Assess for malaria.
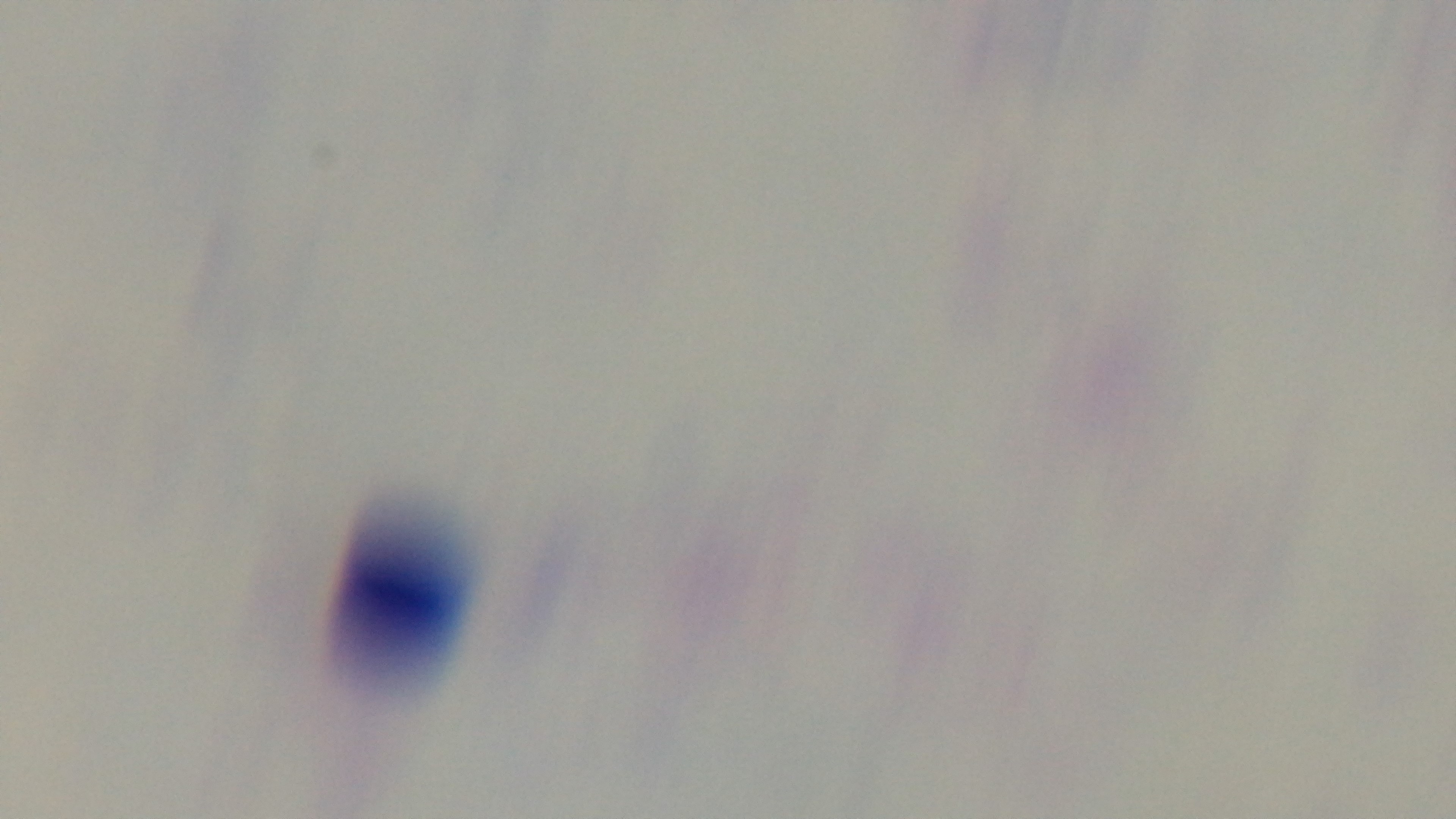
Negative.

Captured with a mounted 4K digital camera. Preparation: thick smear. One field from the slide. Giemsa-stained. 100x oil-immersion objective. Photomicrograph.